Report the malaria status of this cell.
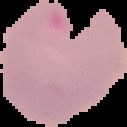
It is parasitized.

image type = segmented cell region on a black background
preparation = thin blood smear
image size = 127×127 pixels